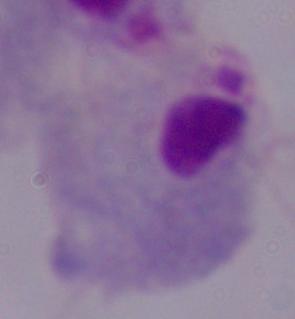
Summary:
  - Modality: photomicrograph
  - Magnification: 1000x
  - Identification: trichomonad